Point out each leukocyte.
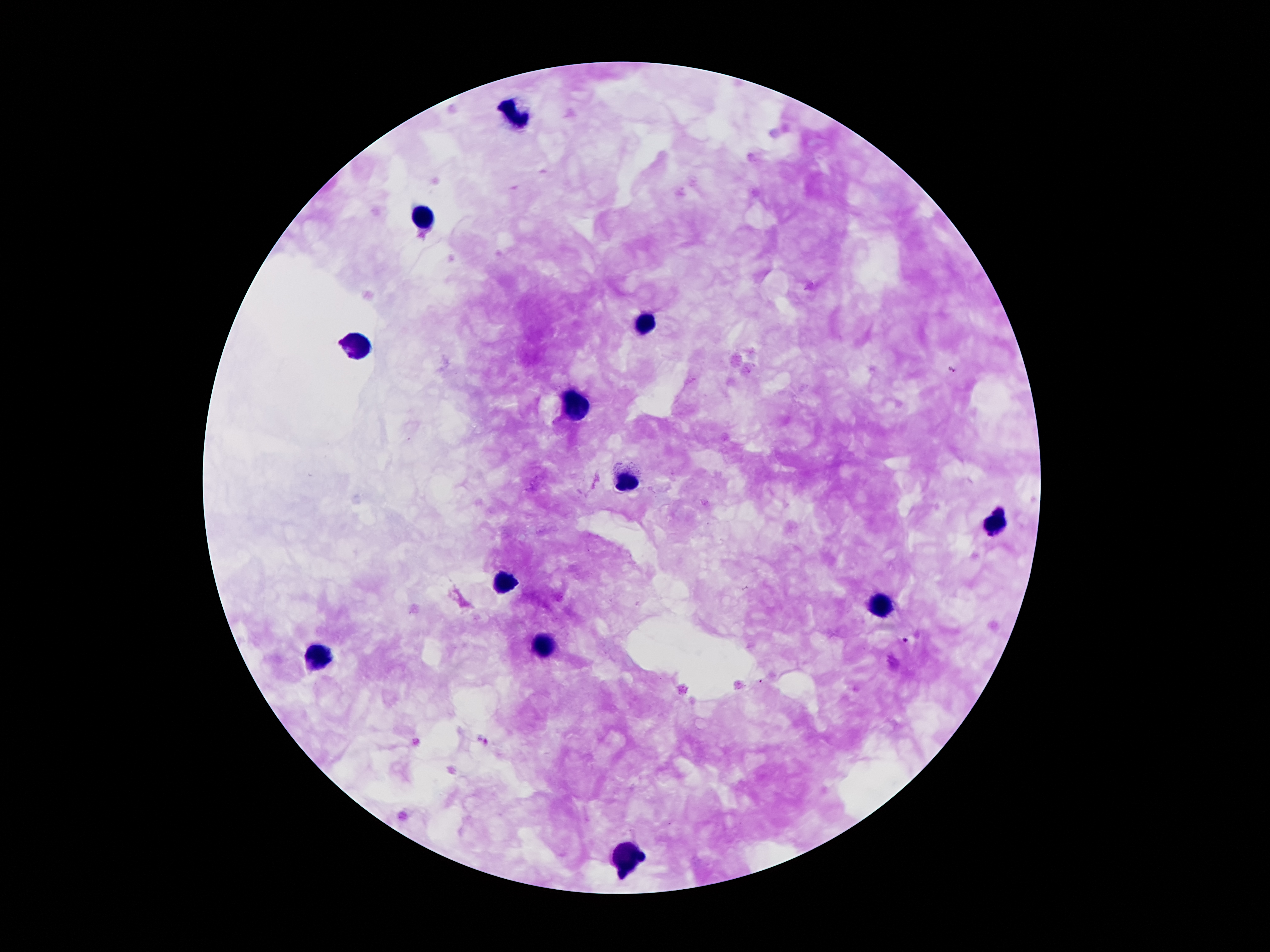

Approximate centers as (x, y) in pixels.
Leukocytes: (519, 116), (424, 218), (645, 325), (361, 346), (576, 406), (624, 482), (998, 524), (504, 581), (880, 604), (544, 646), (311, 656), (634, 856).

Summary:
  - Malaria parasite locations: (952, 369), (906, 640)
  - Field of view: one from this slide
  - Patient malaria status: infected with Plasmodium falciparum
  - Stain: Giemsa
  - Capture: smartphone through the microscope eyepiece
  - Preparation: thick blood film
  - Image size: 1270×952 pixels
  - Magnification: 100x